Comment on the morphology of the erythrocytes.
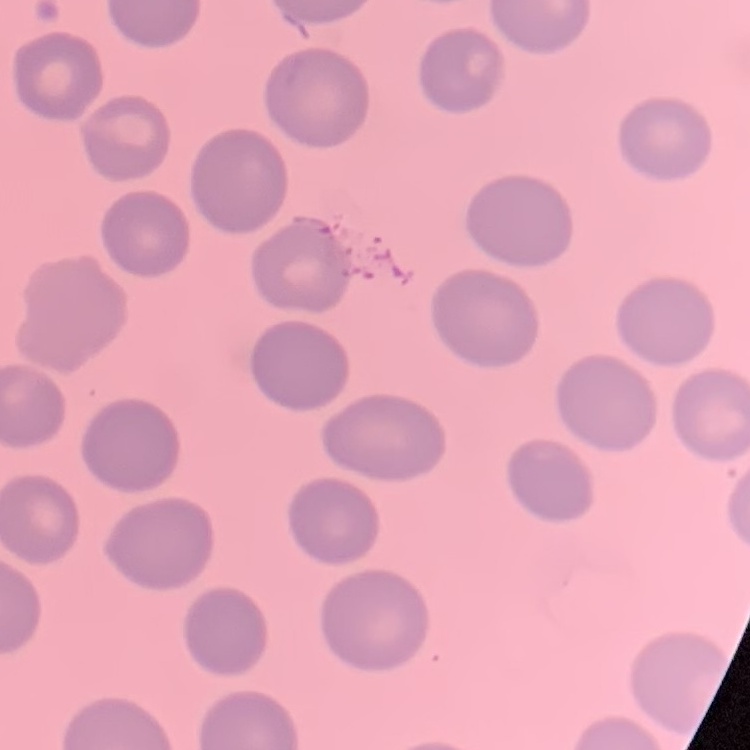

No rouleaux formation.

Summary:
  - Stain: Field's or Giemsa
  - Image type: one tile cut from a larger photomicrograph
  - Preparation: thin peripheral smear